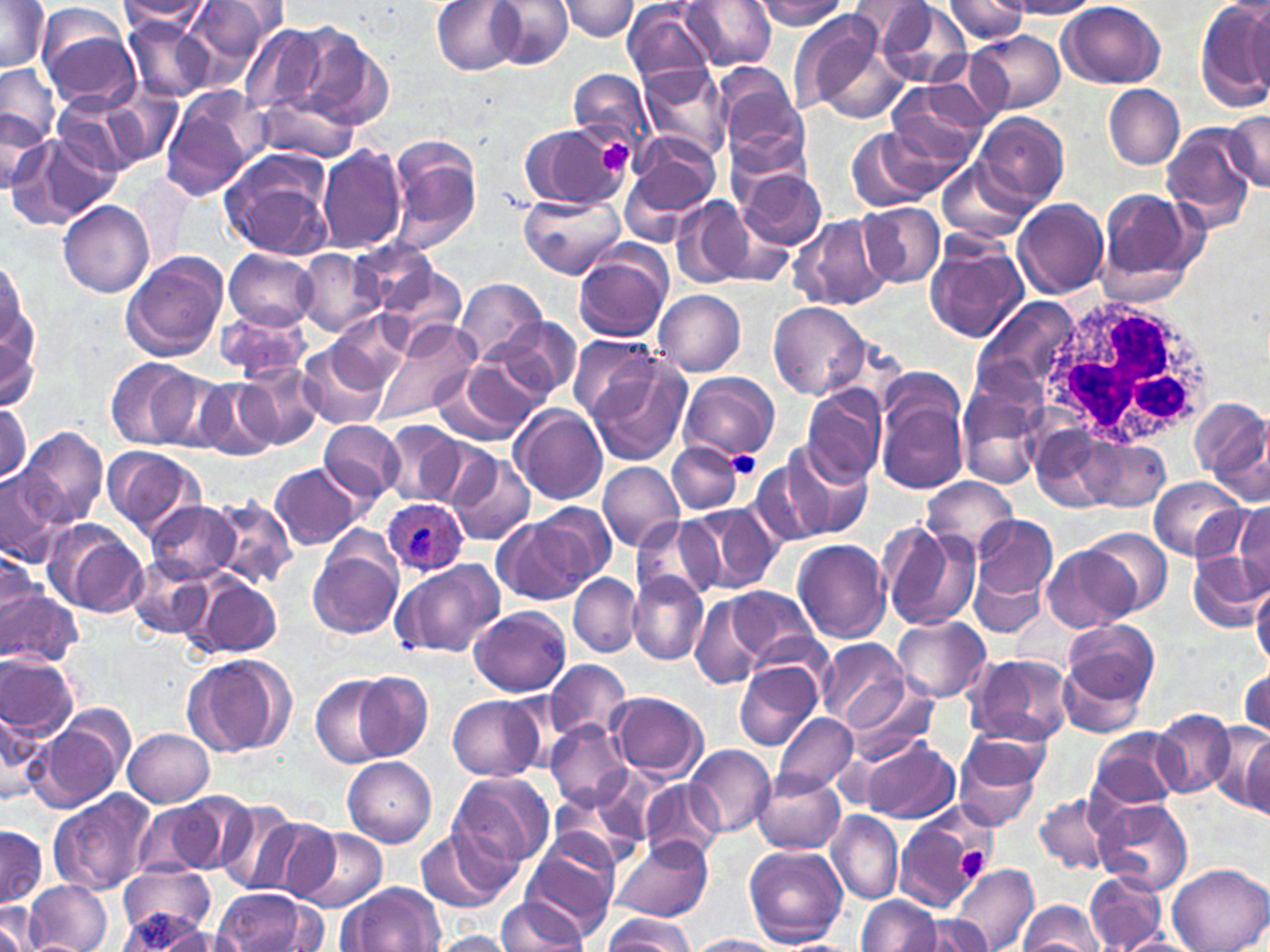
Approximate bounding boxes as named x1/y1/x2/y2 corners in pixels. Uninfected red blood cell locations: (x1=0, y1=0, x2=53, y2=76), (x1=186, y1=0, x2=288, y2=72), (x1=431, y1=0, x2=526, y2=75), (x1=491, y1=0, x2=573, y2=67), (x1=561, y1=0, x2=639, y2=40), (x1=681, y1=0, x2=777, y2=71), (x1=753, y1=0, x2=851, y2=30), (x1=944, y1=0, x2=1031, y2=43), (x1=1196, y1=0, x2=1269, y2=110), (x1=847, y1=1, x2=934, y2=46), (x1=1006, y1=1, x2=1102, y2=17), (x1=871, y1=2, x2=977, y2=88), (x1=1057, y1=2, x2=1166, y2=88), (x1=118, y1=3, x2=213, y2=33), (x1=36, y1=4, x2=140, y2=110), (x1=623, y1=4, x2=715, y2=86), (x1=1246, y1=5, x2=1269, y2=98), (x1=790, y1=8, x2=905, y2=122), (x1=123, y1=18, x2=213, y2=102), (x1=283, y1=20, x2=392, y2=131), (x1=239, y1=24, x2=330, y2=116), (x1=968, y1=30, x2=1063, y2=114), (x1=0, y1=63, x2=60, y2=158), (x1=639, y1=64, x2=732, y2=159), (x1=714, y1=68, x2=809, y2=166), (x1=568, y1=69, x2=651, y2=146), (x1=885, y1=81, x2=989, y2=176), (x1=1104, y1=84, x2=1185, y2=168), (x1=106, y1=86, x2=184, y2=170), (x1=159, y1=90, x2=264, y2=199), (x1=256, y1=92, x2=360, y2=164), (x1=2, y1=105, x2=52, y2=193), (x1=977, y1=112, x2=1068, y2=208), (x1=1225, y1=112, x2=1270, y2=190), (x1=1161, y1=122, x2=1257, y2=230), (x1=518, y1=124, x2=629, y2=210), (x1=845, y1=127, x2=941, y2=213), (x1=23, y1=130, x2=125, y2=231), (x1=623, y1=132, x2=723, y2=227), (x1=387, y1=138, x2=482, y2=251), (x1=318, y1=145, x2=406, y2=254), (x1=219, y1=148, x2=335, y2=261), (x1=937, y1=159, x2=1032, y2=244), (x1=733, y1=164, x2=828, y2=251), (x1=1097, y1=187, x2=1203, y2=298), (x1=519, y1=193, x2=627, y2=279), (x1=669, y1=196, x2=756, y2=291), (x1=1012, y1=198, x2=1109, y2=299), (x1=58, y1=201, x2=154, y2=297), (x1=857, y1=202, x2=945, y2=287), (x1=704, y1=207, x2=793, y2=289), (x1=788, y1=214, x2=892, y2=312), (x1=924, y1=237, x2=1029, y2=344), (x1=352, y1=239, x2=444, y2=316), (x1=573, y1=246, x2=672, y2=342), (x1=223, y1=249, x2=319, y2=330), (x1=292, y1=249, x2=386, y2=337), (x1=121, y1=252, x2=228, y2=362), (x1=2, y1=256, x2=40, y2=401), (x1=379, y1=265, x2=466, y2=347), (x1=455, y1=277, x2=547, y2=366), (x1=655, y1=291, x2=747, y2=377), (x1=970, y1=301, x2=1082, y2=406), (x1=770, y1=302, x2=869, y2=400), (x1=218, y1=307, x2=312, y2=381), (x1=332, y1=314, x2=412, y2=385), (x1=487, y1=317, x2=582, y2=406), (x1=372, y1=321, x2=478, y2=425), (x1=568, y1=336, x2=657, y2=423), (x1=300, y1=343, x2=389, y2=430), (x1=584, y1=356, x2=692, y2=468), (x1=106, y1=358, x2=201, y2=450), (x1=435, y1=358, x2=546, y2=446), (x1=238, y1=364, x2=323, y2=450), (x1=148, y1=370, x2=235, y2=455), (x1=679, y1=372, x2=781, y2=465), (x1=192, y1=377, x2=280, y2=461), (x1=872, y1=377, x2=968, y2=494), (x1=802, y1=385, x2=887, y2=485), (x1=958, y1=390, x2=1044, y2=488), (x1=1191, y1=397, x2=1270, y2=490), (x1=0, y1=400, x2=30, y2=488), (x1=510, y1=404, x2=608, y2=505), (x1=318, y1=419, x2=405, y2=502), (x1=382, y1=420, x2=465, y2=507), (x1=19, y1=425, x2=107, y2=528), (x1=414, y1=434, x2=498, y2=508), (x1=1070, y1=436, x2=1179, y2=512), (x1=668, y1=443, x2=744, y2=514), (x1=785, y1=444, x2=877, y2=540), (x1=102, y1=445, x2=206, y2=542), (x1=747, y1=448, x2=844, y2=546), (x1=445, y1=449, x2=536, y2=547), (x1=598, y1=461, x2=684, y2=553), (x1=269, y1=463, x2=362, y2=550), (x1=0, y1=468, x2=68, y2=565), (x1=922, y1=477, x2=1020, y2=561), (x1=1149, y1=477, x2=1245, y2=561), (x1=207, y1=496, x2=297, y2=587), (x1=144, y1=500, x2=240, y2=581), (x1=1233, y1=501, x2=1270, y2=592), (x1=535, y1=502, x2=617, y2=584), (x1=685, y1=503, x2=780, y2=592), (x1=970, y1=514, x2=1058, y2=620), (x1=633, y1=517, x2=718, y2=603), (x1=493, y1=518, x2=590, y2=605), (x1=878, y1=522, x2=980, y2=630), (x1=56, y1=523, x2=150, y2=618), (x1=1084, y1=529, x2=1172, y2=615), (x1=792, y1=538, x2=891, y2=644), (x1=309, y1=541, x2=401, y2=639), (x1=1044, y1=547, x2=1136, y2=634), (x1=1186, y1=549, x2=1267, y2=631), (x1=0, y1=550, x2=45, y2=636), (x1=127, y1=555, x2=212, y2=638), (x1=389, y1=559, x2=506, y2=660), (x1=970, y1=560, x2=1047, y2=639), (x1=629, y1=572, x2=708, y2=665), (x1=570, y1=574, x2=640, y2=655), (x1=193, y1=575, x2=283, y2=658), (x1=1252, y1=581, x2=1270, y2=669), (x1=719, y1=584, x2=820, y2=669), (x1=0, y1=589, x2=79, y2=665), (x1=686, y1=592, x2=778, y2=688), (x1=470, y1=606, x2=571, y2=697), (x1=891, y1=615, x2=991, y2=702), (x1=1063, y1=619, x2=1158, y2=705), (x1=816, y1=639, x2=907, y2=730), (x1=1058, y1=647, x2=1154, y2=741), (x1=0, y1=652, x2=78, y2=742), (x1=964, y1=653, x2=1076, y2=747), (x1=185, y1=654, x2=295, y2=758), (x1=546, y1=660, x2=631, y2=741), (x1=735, y1=660, x2=824, y2=751), (x1=1238, y1=667, x2=1269, y2=742), (x1=352, y1=672, x2=432, y2=762), (x1=311, y1=675, x2=396, y2=767), (x1=837, y1=676, x2=940, y2=770), (x1=611, y1=692, x2=709, y2=780), (x1=449, y1=695, x2=545, y2=780), (x1=1, y1=706, x2=44, y2=807), (x1=33, y1=709, x2=133, y2=812), (x1=1152, y1=709, x2=1236, y2=799), (x1=771, y1=712, x2=858, y2=792), (x1=962, y1=717, x2=1052, y2=788), (x1=547, y1=721, x2=633, y2=810), (x1=1223, y1=724, x2=1269, y2=816), (x1=123, y1=728, x2=214, y2=806), (x1=1088, y1=729, x2=1184, y2=812), (x1=952, y1=730, x2=1047, y2=831), (x1=863, y1=738, x2=959, y2=825), (x1=686, y1=744, x2=775, y2=836), (x1=343, y1=756, x2=436, y2=846), (x1=752, y1=769, x2=846, y2=855), (x1=449, y1=771, x2=555, y2=871), (x1=641, y1=780, x2=723, y2=865), (x1=552, y1=783, x2=646, y2=868), (x1=49, y1=791, x2=156, y2=895), (x1=1034, y1=792, x2=1119, y2=876), (x1=1093, y1=798, x2=1193, y2=896), (x1=133, y1=799, x2=224, y2=879), (x1=213, y1=801, x2=311, y2=897), (x1=826, y1=811, x2=903, y2=907), (x1=893, y1=814, x2=985, y2=911), (x1=0, y1=825, x2=50, y2=910), (x1=291, y1=827, x2=387, y2=912), (x1=415, y1=827, x2=516, y2=914), (x1=521, y1=832, x2=620, y2=940), (x1=612, y1=835, x2=712, y2=922), (x1=743, y1=845, x2=848, y2=948), (x1=118, y1=862, x2=215, y2=945), (x1=951, y1=862, x2=1039, y2=952), (x1=1168, y1=864, x2=1270, y2=951), (x1=1085, y1=870, x2=1168, y2=950), (x1=26, y1=881, x2=112, y2=952), (x1=339, y1=883, x2=444, y2=952), (x1=213, y1=888, x2=319, y2=952), (x1=857, y1=895, x2=939, y2=951), (x1=496, y1=898, x2=591, y2=950), (x1=1016, y1=899, x2=1105, y2=950), (x1=0, y1=903, x2=43, y2=952), (x1=604, y1=912, x2=694, y2=951), (x1=117, y1=914, x2=211, y2=949), (x1=912, y1=915, x2=993, y2=952), (x1=147, y1=924, x2=250, y2=952), (x1=1109, y1=931, x2=1200, y2=951), (x1=424, y1=932, x2=518, y2=952), (x1=687, y1=935, x2=787, y2=952). Plasmodium ovale-infected red blood cell locations: (x1=381, y1=497, x2=468, y2=576). White blood cell locations: (x1=1042, y1=294, x2=1219, y2=447). Platelet locations: (x1=590, y1=136, x2=634, y2=176), (x1=728, y1=451, x2=759, y2=477), (x1=953, y1=845, x2=992, y2=883). Slide-level diagnosis: Plasmodium ovale. May-Grünwald-Giemsa-stained preparation. Image is 1270×952 pixels. Thin blood smear. 1000x magnification. Single field of view. Optical microscopy.